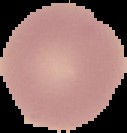
preparation = thin blood film
result = negative for Plasmodium parasites
image type = segmented cell region on a black background
image size = 127×133 pixels